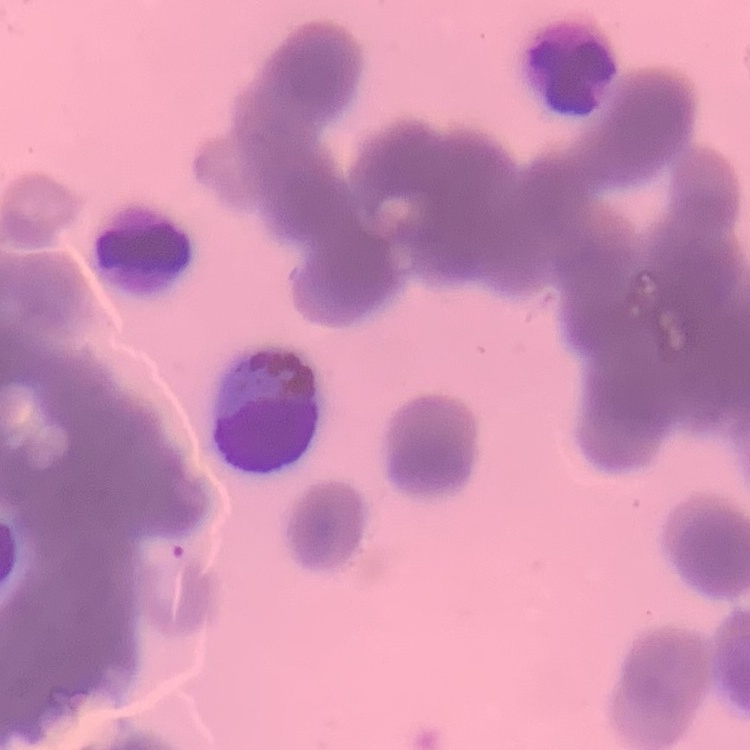
Summary:
  - Erythrocyte morphology: rouleaux formation
  - Preparation: thin peripheral smear
  - Image type: one tile cut from a larger photomicrograph
  - Stain: Field's or Giemsa